Assess this cell for malaria.
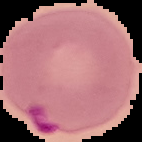
Parasitized.

image size = 142×142 pixels
preparation = thin blood film
image type = segmented cell region with the area outside set to black